State which parasite is depicted.
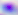

Toxoplasma gondii.

Photomicrograph. Captured at 400x magnification.